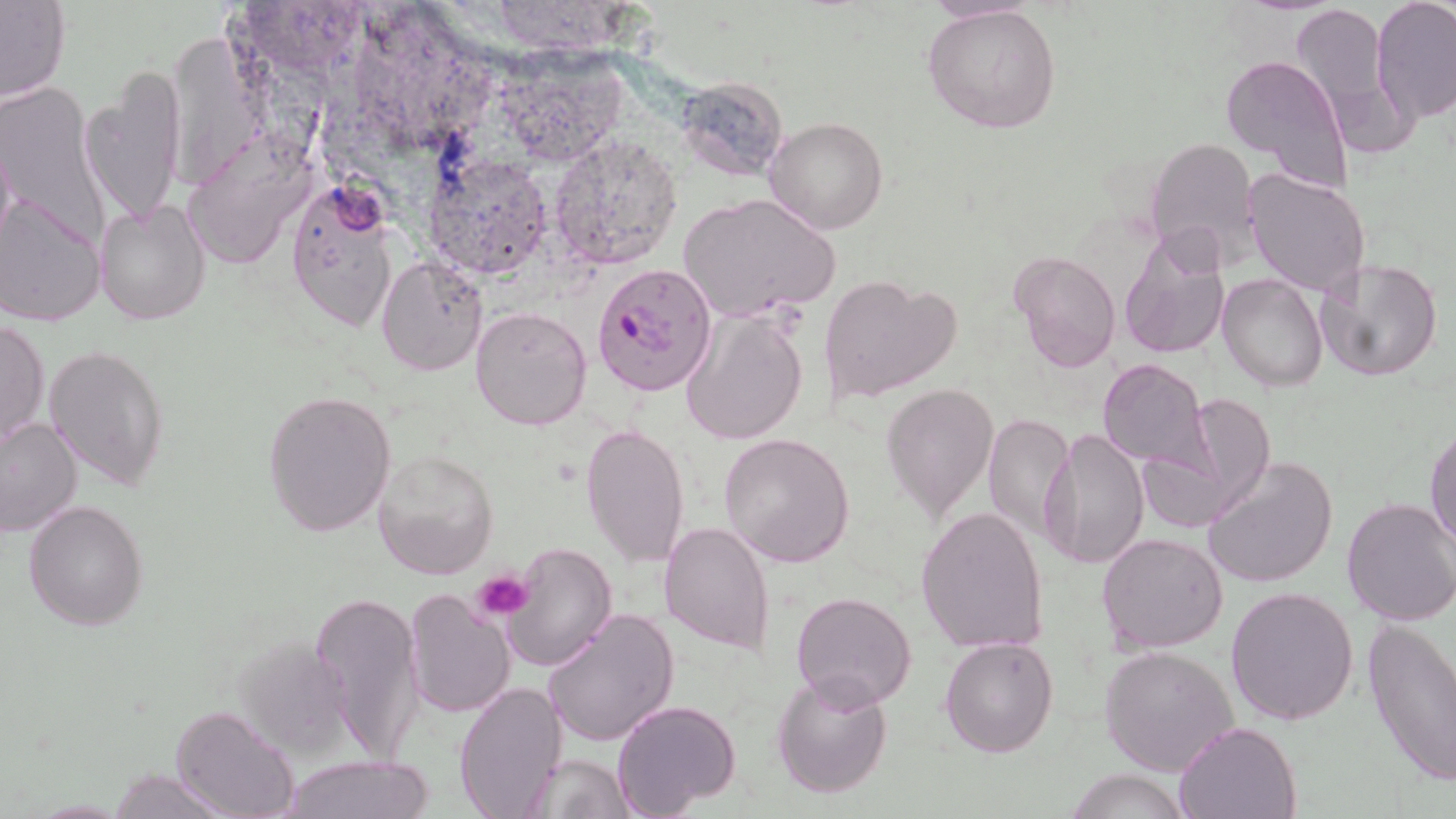
Summary:
  - Coordinate format: approximate bounding boxes as (x1,y1)-(x2,y2) corner pairs in pixels
  - Plasmodium falciparum-infected red blood cell locations: (590,261)-(718,398)
  - Uninfected red blood cell locations: (1289,0)-(1408,143), (1370,0)-(1456,124), (0,3)-(71,103), (920,5)-(1064,134), (1218,53)-(1352,192), (81,73)-(186,225), (675,77)-(790,179), (0,85)-(112,254), (765,116)-(889,234), (552,135)-(684,269), (1146,136)-(1262,272), (182,141)-(310,271), (426,154)-(556,275), (1243,168)-(1370,296), (287,180)-(399,329), (679,192)-(840,327), (1,193)-(105,327), (95,197)-(212,324), (1118,231)-(1233,362), (1011,249)-(1121,372), (376,258)-(487,375), (1312,258)-(1444,384), (818,274)-(961,403), (1218,276)-(1328,391), (472,305)-(592,431), (681,310)-(808,445), (1,317)-(48,447), (45,343)-(168,491), (1098,358)-(1212,471), (880,382)-(999,520), (262,389)-(398,538), (1183,392)-(1274,518), (981,414)-(1073,546), (0,416)-(83,539), (579,421)-(691,567), (1039,425)-(1150,572), (1426,425)-(1456,554), (720,432)-(854,568), (371,448)-(499,580), (1203,458)-(1338,589), (1339,496)-(1456,626), (25,499)-(148,631), (916,507)-(1048,654), (660,521)-(775,654), (1095,531)-(1229,655), (505,542)-(617,673), (1226,585)-(1360,726), (403,586)-(516,720), (309,589)-(425,763), (790,591)-(916,710), (542,607)-(680,748), (1362,617)-(1456,786), (939,636)-(1059,757), (1100,645)-(1239,777), (770,669)-(893,799), (453,677)-(566,818), (611,698)-(742,817), (172,704)-(298,819), (1173,721)-(1303,819), (281,753)-(434,819), (520,753)-(635,819), (1067,767)-(1190,819), (107,769)-(231,818)
  - Platelet locations: (472,569)-(534,620)
  - Slide-level diagnosis: Plasmodium falciparum
  - Field of view: single
  - Modality: light microscopy
  - Image size: 1456×819 pixels
  - Stain: May-Grünwald-Giemsa
  - Magnification: 1000x
  - Preparation: thin blood smear